Identify the parasite.
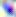

This is Toxoplasma gondii.

Summary:
  - Magnification: 400x
  - Modality: micrograph